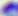 400x magnification. Toxoplasma gondii is seen. Photomicrograph.